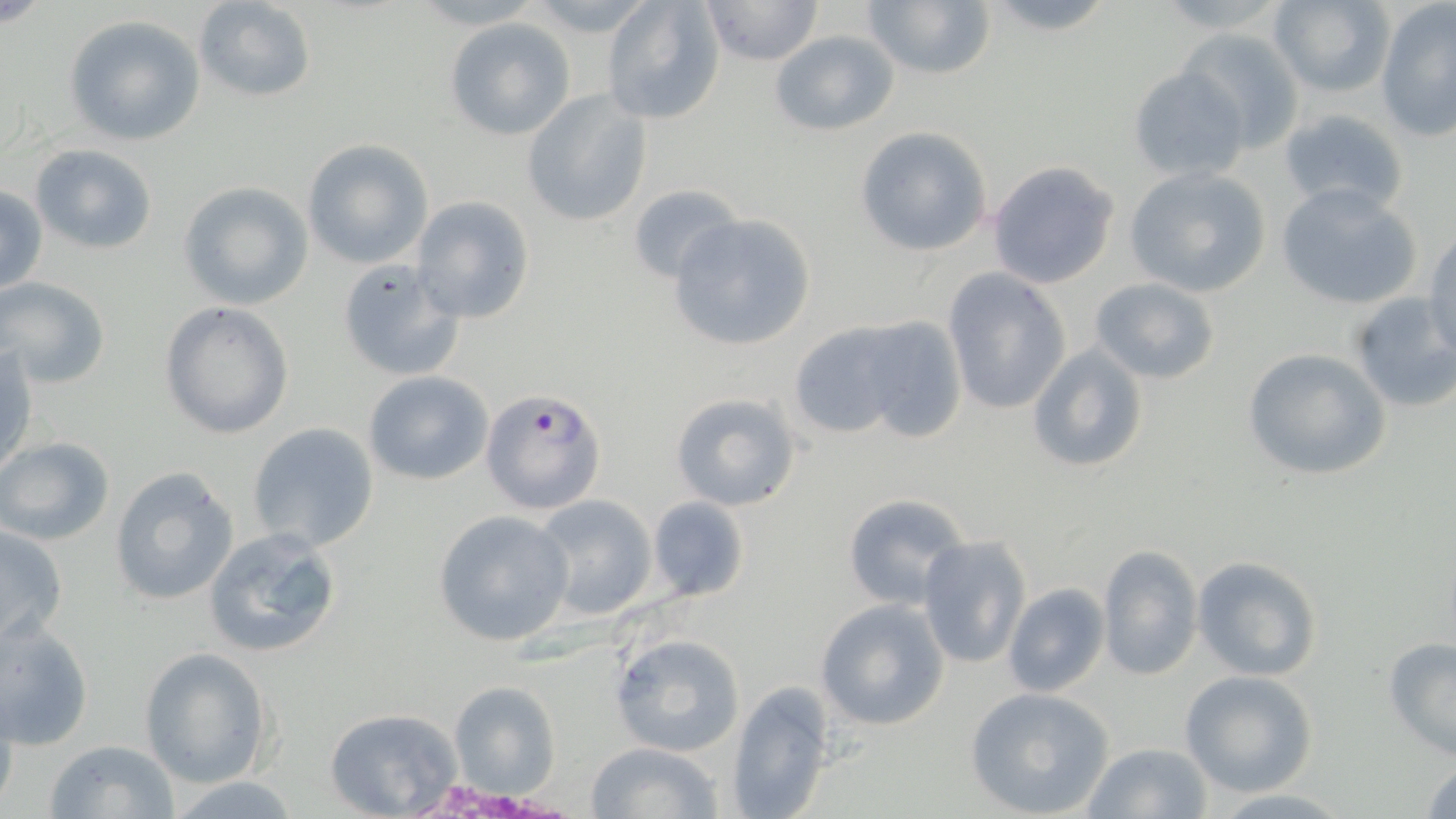

Summary:
  - Coordinate format: approximate bounding boxes as (x1, y1, x2, y2) in pixels
  - Plasmodium falciparum-infected red blood cell locations: (481, 386, 606, 515)
  - Uninfected red blood cell locations: (601, 0, 725, 125), (699, 0, 823, 67), (861, 0, 997, 82), (976, 0, 1120, 36), (1266, 0, 1397, 96), (192, 1, 317, 104), (1376, 4, 1456, 141), (65, 15, 205, 146), (444, 19, 575, 139), (1178, 27, 1306, 152), (768, 29, 900, 136), (1129, 65, 1251, 184), (520, 92, 652, 226), (1277, 106, 1410, 218), (855, 127, 991, 255), (301, 139, 434, 268), (29, 143, 158, 255), (986, 159, 1121, 289), (1123, 166, 1272, 298), (623, 181, 740, 288), (176, 182, 312, 310), (1275, 184, 1425, 310), (0, 186, 47, 297), (410, 195, 536, 323), (667, 213, 815, 352), (1425, 232, 1456, 364), (336, 259, 466, 382), (942, 267, 1072, 418), (1, 276, 111, 389), (1088, 276, 1221, 384), (1348, 293, 1456, 414), (158, 301, 295, 439), (852, 315, 969, 443), (786, 319, 916, 439), (1026, 340, 1150, 474), (1242, 347, 1390, 481), (1, 348, 38, 482), (361, 371, 493, 488), (669, 391, 801, 512), (247, 421, 380, 553), (0, 436, 115, 548), (108, 468, 238, 607), (841, 492, 972, 611), (533, 493, 657, 619), (647, 496, 750, 602), (432, 509, 574, 647), (1, 523, 70, 647), (204, 527, 343, 658), (916, 535, 1031, 669), (1096, 545, 1202, 680), (1193, 556, 1323, 681), (1001, 583, 1110, 697), (814, 598, 952, 731), (0, 620, 96, 751), (611, 633, 747, 756), (1382, 638, 1456, 760), (139, 647, 274, 788), (1179, 670, 1318, 796), (448, 681, 561, 798), (0, 684, 20, 816), (726, 684, 835, 819), (965, 687, 1116, 817), (324, 708, 467, 818), (44, 738, 182, 819), (586, 741, 725, 819), (1082, 742, 1212, 819), (1421, 757, 1456, 817), (166, 776, 306, 816), (1207, 789, 1354, 819)
  - Slide-level diagnosis: Plasmodium falciparum
  - Stain: May-Grünwald-Giemsa
  - Image size: 1456×819 pixels
  - Magnification: 1000x
  - Field of view: single
  - Preparation: thin blood film
  - Modality: light microscopy